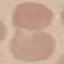
malaria_status: uninfected
capture: smartphone camera at the microscope eyepiece
image_type: cell patch, automatically extracted from a larger field of view and resized to 64 × 64 pixels
stain: Giemsa
preparation: thin blood smear